Classify this cell by malaria status.
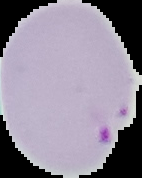
It is parasitized.

From a thin blood smear. Image is 142×178 pixels. Segmented cell region on a black background.